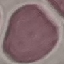
Summary:
  - Result: no malaria parasites seen
  - Preparation: thin blood smear
  - Capture: smartphone camera at the microscope eyepiece
  - Image type: cell patch, automatically extracted from a larger field of view and resized to 64 × 64 pixels
  - Stain: Giemsa